Report the malaria status of this cell.
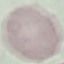

Uninfected.

Acquired by smartphone through the microscope eyepiece. Cell patch, automatically extracted from a larger field of view and resized to 64 × 64 pixels. Giemsa-stained preparation. Thin smear of blood.